State the blood parasite species.
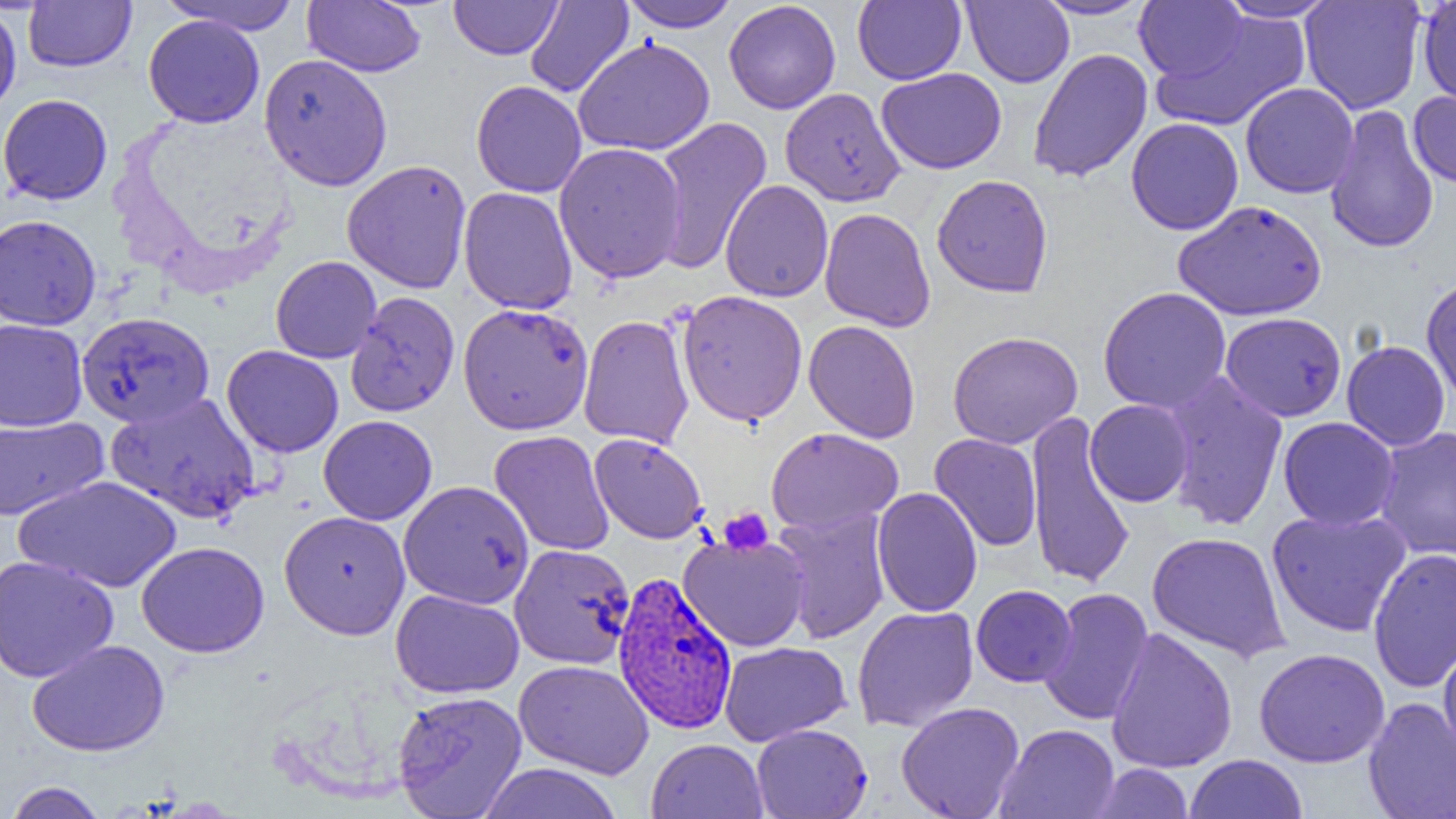

Plasmodium vivax.

Approximate bounding boxes as named x1/y1/x2/y2 corners in pixels. Platelet locations: (x1=718, y1=507, x2=774, y2=555). Uninfected red blood cell locations: (x1=24, y1=0, x2=136, y2=73), (x1=159, y1=0, x2=303, y2=34), (x1=449, y1=0, x2=562, y2=60), (x1=620, y1=0, x2=740, y2=32), (x1=723, y1=0, x2=841, y2=114), (x1=852, y1=0, x2=966, y2=85), (x1=962, y1=0, x2=1074, y2=88), (x1=1033, y1=0, x2=1155, y2=20), (x1=1300, y1=0, x2=1426, y2=114), (x1=1417, y1=0, x2=1456, y2=108), (x1=303, y1=1, x2=426, y2=77), (x1=525, y1=1, x2=634, y2=98), (x1=1134, y1=1, x2=1247, y2=81), (x1=1214, y1=1, x2=1339, y2=22), (x1=0, y1=4, x2=22, y2=117), (x1=1150, y1=10, x2=1310, y2=133), (x1=143, y1=14, x2=264, y2=127), (x1=573, y1=37, x2=715, y2=156), (x1=1027, y1=48, x2=1153, y2=183), (x1=258, y1=53, x2=393, y2=191), (x1=876, y1=68, x2=1007, y2=174), (x1=471, y1=80, x2=587, y2=197), (x1=1240, y1=82, x2=1359, y2=199), (x1=780, y1=87, x2=906, y2=207), (x1=1408, y1=90, x2=1456, y2=189), (x1=0, y1=93, x2=113, y2=205), (x1=1325, y1=104, x2=1439, y2=254), (x1=651, y1=116, x2=773, y2=274), (x1=1126, y1=117, x2=1244, y2=235), (x1=553, y1=142, x2=687, y2=284), (x1=341, y1=159, x2=472, y2=294), (x1=931, y1=174, x2=1054, y2=297), (x1=720, y1=179, x2=834, y2=302), (x1=458, y1=186, x2=578, y2=315), (x1=1174, y1=200, x2=1327, y2=321), (x1=819, y1=207, x2=936, y2=332), (x1=0, y1=214, x2=101, y2=331), (x1=270, y1=256, x2=382, y2=363), (x1=1421, y1=274, x2=1456, y2=404), (x1=1098, y1=286, x2=1232, y2=414), (x1=676, y1=290, x2=808, y2=426), (x1=345, y1=291, x2=460, y2=417), (x1=457, y1=303, x2=594, y2=436), (x1=77, y1=311, x2=214, y2=429), (x1=1220, y1=312, x2=1347, y2=422), (x1=577, y1=314, x2=694, y2=449), (x1=0, y1=318, x2=88, y2=431), (x1=804, y1=320, x2=921, y2=444), (x1=947, y1=331, x2=1083, y2=449), (x1=1342, y1=340, x2=1450, y2=451), (x1=222, y1=345, x2=344, y2=458), (x1=1161, y1=372, x2=1289, y2=531), (x1=107, y1=391, x2=261, y2=524), (x1=1085, y1=399, x2=1194, y2=507), (x1=1025, y1=411, x2=1136, y2=589), (x1=0, y1=415, x2=108, y2=522), (x1=318, y1=415, x2=438, y2=525), (x1=1278, y1=417, x2=1399, y2=531), (x1=766, y1=427, x2=903, y2=535), (x1=1374, y1=427, x2=1456, y2=561), (x1=489, y1=430, x2=614, y2=557), (x1=589, y1=433, x2=708, y2=544), (x1=929, y1=433, x2=1043, y2=551), (x1=16, y1=475, x2=182, y2=593), (x1=398, y1=480, x2=535, y2=609), (x1=871, y1=487, x2=983, y2=617), (x1=772, y1=508, x2=892, y2=644), (x1=1267, y1=508, x2=1412, y2=638), (x1=279, y1=511, x2=411, y2=639), (x1=1146, y1=531, x2=1290, y2=662), (x1=678, y1=535, x2=810, y2=651), (x1=137, y1=541, x2=269, y2=657), (x1=509, y1=543, x2=635, y2=669), (x1=1368, y1=548, x2=1456, y2=692), (x1=0, y1=555, x2=119, y2=683), (x1=971, y1=584, x2=1077, y2=687), (x1=1038, y1=587, x2=1154, y2=725), (x1=391, y1=589, x2=525, y2=698), (x1=852, y1=605, x2=979, y2=732), (x1=1105, y1=627, x2=1238, y2=774), (x1=1438, y1=638, x2=1456, y2=764), (x1=27, y1=639, x2=169, y2=757), (x1=720, y1=641, x2=851, y2=745), (x1=1253, y1=648, x2=1390, y2=768), (x1=514, y1=659, x2=654, y2=779), (x1=392, y1=690, x2=527, y2=819), (x1=1363, y1=698, x2=1456, y2=819), (x1=896, y1=701, x2=1025, y2=819), (x1=751, y1=723, x2=872, y2=818), (x1=995, y1=723, x2=1120, y2=818), (x1=646, y1=738, x2=768, y2=819), (x1=1184, y1=754, x2=1308, y2=819), (x1=476, y1=762, x2=625, y2=818), (x1=1091, y1=763, x2=1195, y2=818), (x1=3, y1=781, x2=109, y2=819). Plasmodium vivax-infected red blood cell locations: (x1=612, y1=571, x2=738, y2=735). Thin blood film. Light microscopy. Image is 1456×819 pixels. 1000x magnification. Single field of view.